Give the position of every Plasmodium parasite.
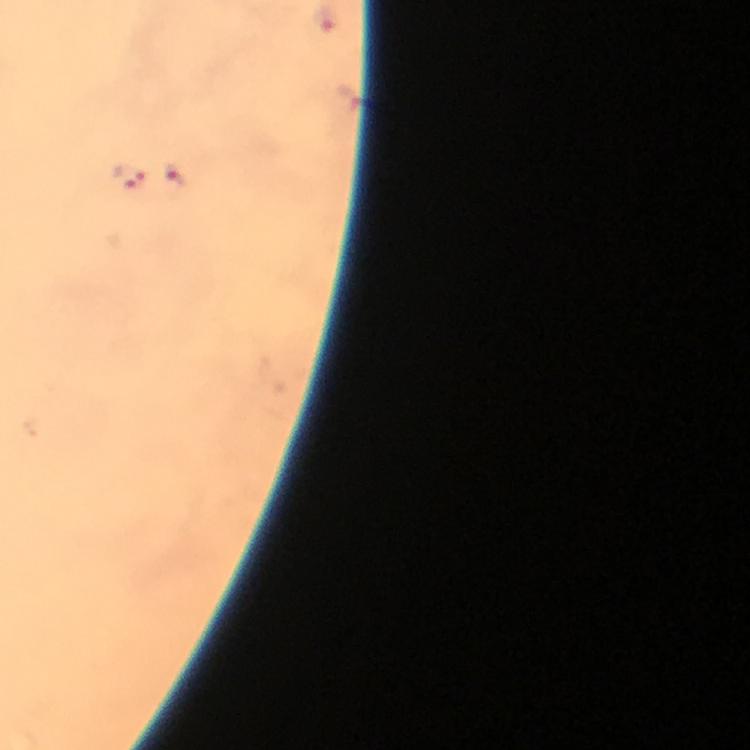
Approximate centers as (x, y) in pixels.
Plasmodium parasites: (327, 22), (176, 175), (130, 178).

image size = 750×750 pixels
context = from a diagnostic examination for malaria
stain = Giemsa
capture = smartphone mounted on the microscope
immersion oil = used
preparation = thick blood film
cropped from = a single field of view
magnification = 100x